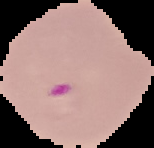

image type = cell region segmented out of the field of view; surrounding area masked to black
preparation = thin blood smear
image size = 154×148 pixels
result = Plasmodium parasites identified